Classify this cell by malaria status.
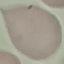
Uninfected.

capture = smartphone through the microscope eyepiece
image type = cell patch, automatically extracted from a larger field of view and resized to 64 × 64 pixels
stain = Giemsa
preparation = thin smear